Outline each blood parasite and name the species.
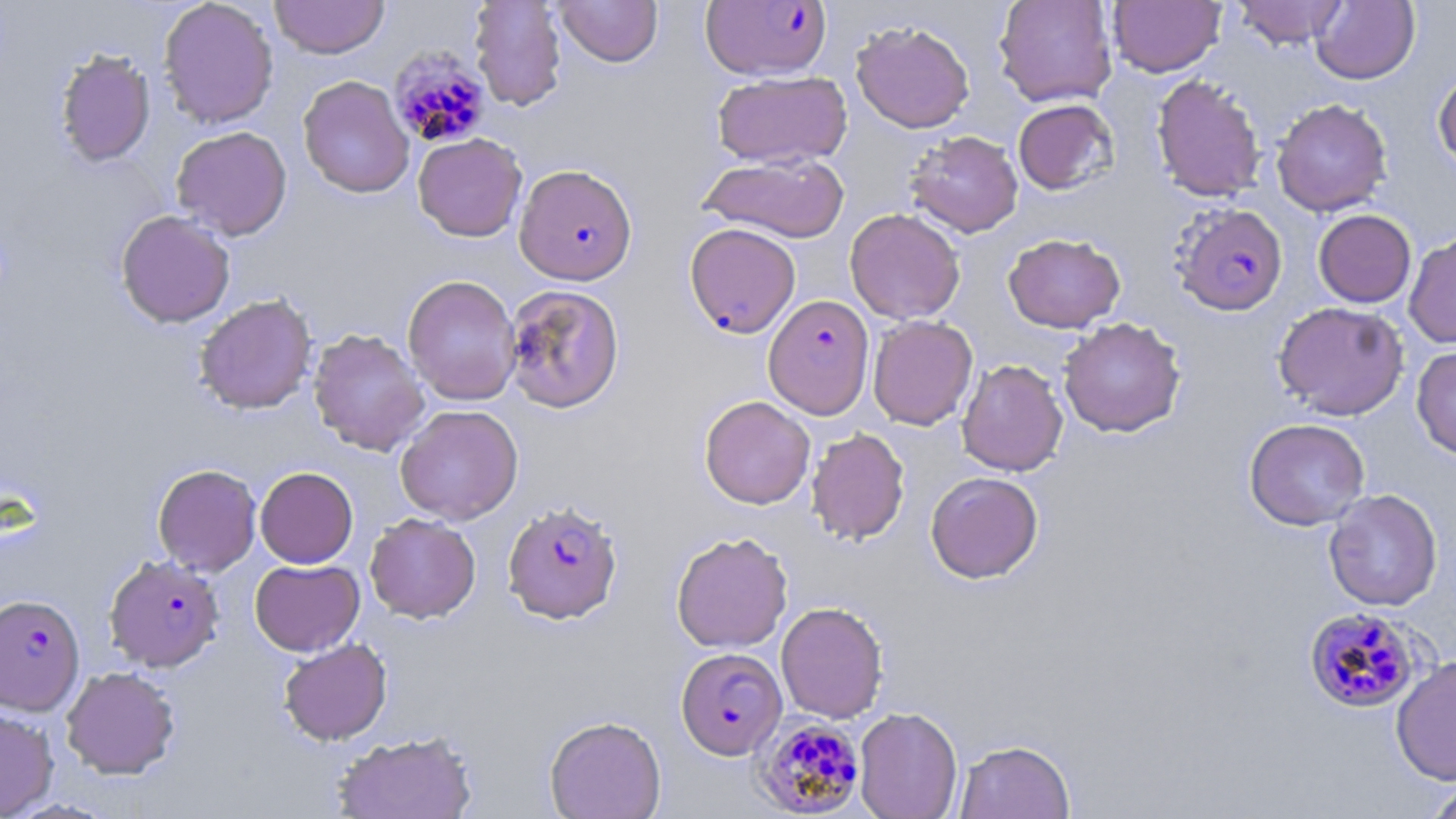

Approximate bounding boxes as [x1, y1, x2, y2] in pixels.
Plasmodium falciparum-infected red blood cells: [700, 1, 832, 80], [389, 47, 492, 150], [513, 164, 638, 285], [1171, 203, 1289, 317], [684, 222, 801, 339], [763, 295, 874, 419], [502, 500, 622, 624], [101, 557, 222, 674], [0, 594, 85, 714], [1303, 607, 1422, 713], [676, 647, 787, 760], [754, 717, 866, 816].
No Plasmodium ovale, Plasmodium malariae, Plasmodium vivax, Babesia divergens, or Trypanosoma brucei observed.

Summary:
  - Uninfected red blood cell locations: [158, 0, 279, 129], [269, 0, 390, 59], [469, 0, 567, 111], [554, 0, 663, 67], [994, 0, 1117, 107], [1108, 0, 1225, 77], [1231, 0, 1350, 49], [1311, 0, 1420, 85], [851, 20, 975, 133], [54, 48, 156, 168], [1432, 68, 1456, 171], [712, 70, 851, 168], [1151, 74, 1267, 202], [298, 75, 414, 198], [1149, 89, 1393, 204], [1271, 98, 1392, 216], [1013, 99, 1119, 195], [170, 126, 293, 240], [905, 130, 1023, 238], [413, 133, 527, 241], [698, 153, 850, 243], [845, 208, 965, 324], [1313, 209, 1416, 308], [116, 210, 235, 328], [1404, 232, 1456, 348], [1003, 233, 1126, 333], [402, 274, 522, 405], [503, 284, 625, 413], [194, 294, 317, 414], [1272, 301, 1409, 421], [868, 315, 978, 430], [1058, 317, 1186, 438], [308, 328, 430, 456], [1411, 345, 1456, 460], [957, 359, 1068, 476], [699, 395, 815, 509], [395, 404, 523, 525], [1244, 418, 1369, 530], [806, 427, 910, 545], [152, 463, 262, 575], [255, 466, 358, 568], [925, 471, 1044, 584], [1323, 489, 1443, 612], [365, 513, 481, 622], [671, 531, 793, 653], [249, 559, 364, 655], [776, 601, 889, 723], [278, 638, 392, 745], [1391, 655, 1456, 786], [61, 666, 180, 779], [0, 706, 59, 818], [854, 707, 963, 819], [544, 715, 666, 819], [332, 729, 479, 819], [955, 739, 1075, 819], [1422, 778, 1456, 819]
  - Slide-level diagnosis: Plasmodium falciparum
  - Field of view: one of a larger specimen
  - Magnification: 1000x
  - Modality: light microscopy
  - Preparation: thin blood smear
  - Stain: May-Grünwald-Giemsa
  - Image size: 1456×819 pixels